Locate platelets.
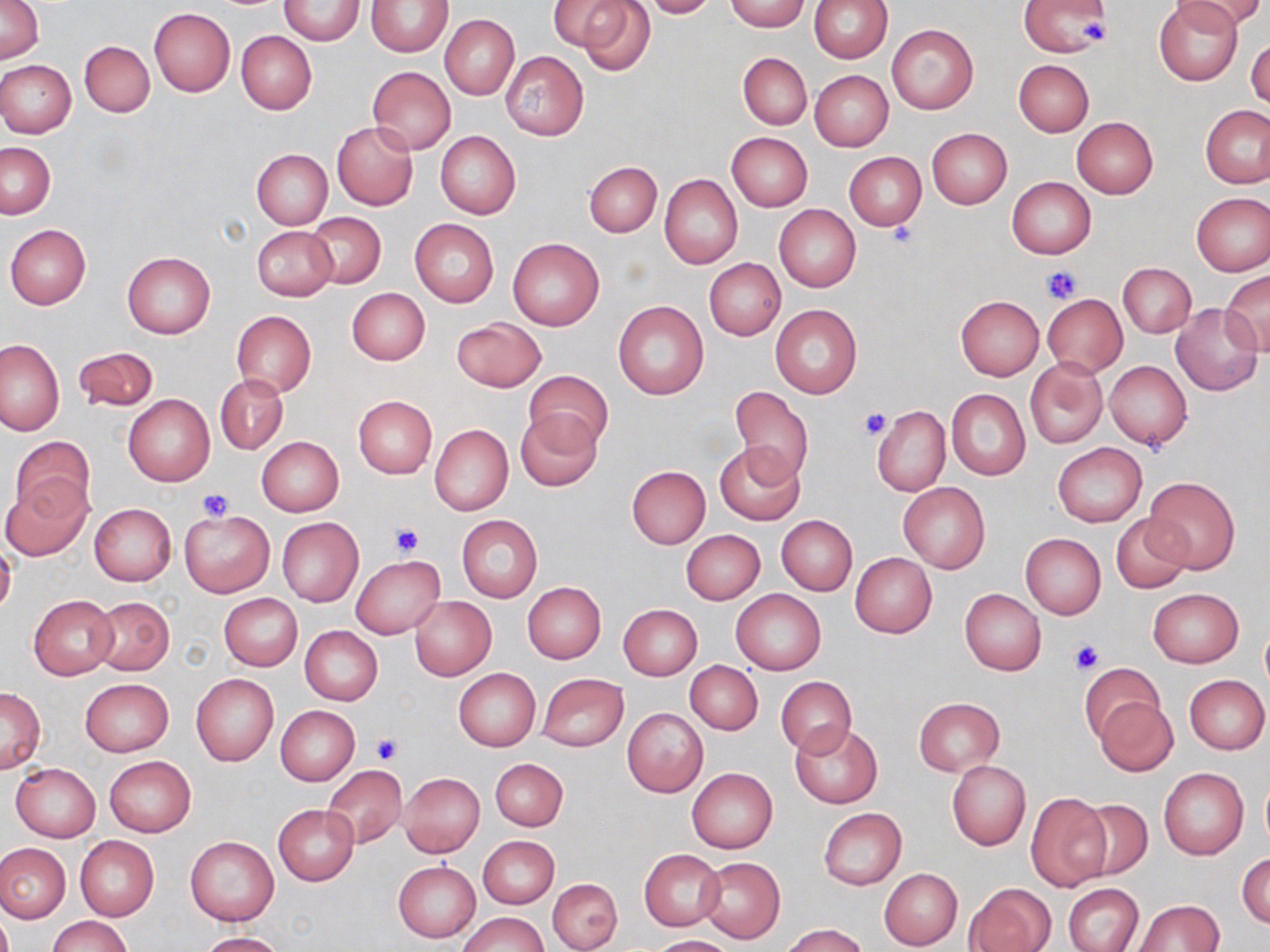

Approximate bounding boxes as named x1/y1/x2/y2 corners in pixels.
Platelets: (x1=1080, y1=18, x2=1107, y2=48), (x1=884, y1=223, x2=919, y2=251), (x1=1040, y1=264, x2=1081, y2=305), (x1=858, y1=408, x2=891, y2=441), (x1=199, y1=488, x2=233, y2=521), (x1=392, y1=523, x2=423, y2=556), (x1=1069, y1=640, x2=1104, y2=676), (x1=371, y1=734, x2=402, y2=764).

Summary:
  - Uninfected red blood cell locations: (x1=1, y1=0, x2=43, y2=64), (x1=278, y1=0, x2=366, y2=45), (x1=548, y1=0, x2=629, y2=52), (x1=576, y1=0, x2=656, y2=77), (x1=642, y1=0, x2=716, y2=18), (x1=723, y1=0, x2=810, y2=32), (x1=809, y1=0, x2=893, y2=62), (x1=1019, y1=0, x2=1114, y2=56), (x1=1177, y1=0, x2=1260, y2=34), (x1=366, y1=1, x2=451, y2=57), (x1=1152, y1=1, x2=1244, y2=85), (x1=149, y1=8, x2=235, y2=96), (x1=440, y1=15, x2=519, y2=99), (x1=887, y1=24, x2=978, y2=114), (x1=235, y1=30, x2=317, y2=114), (x1=1247, y1=34, x2=1269, y2=111), (x1=80, y1=41, x2=155, y2=117), (x1=501, y1=51, x2=589, y2=140), (x1=737, y1=53, x2=811, y2=128), (x1=0, y1=59, x2=76, y2=137), (x1=1014, y1=59, x2=1093, y2=136), (x1=367, y1=66, x2=456, y2=153), (x1=810, y1=70, x2=893, y2=151), (x1=1201, y1=106, x2=1269, y2=188), (x1=1071, y1=116, x2=1158, y2=198), (x1=331, y1=122, x2=419, y2=210), (x1=926, y1=127, x2=1012, y2=208), (x1=435, y1=132, x2=520, y2=219), (x1=727, y1=132, x2=812, y2=211), (x1=1, y1=142, x2=56, y2=218), (x1=252, y1=149, x2=332, y2=228), (x1=844, y1=152, x2=926, y2=229), (x1=583, y1=161, x2=662, y2=237), (x1=660, y1=174, x2=742, y2=268), (x1=1006, y1=177, x2=1096, y2=259), (x1=1192, y1=192, x2=1270, y2=276), (x1=774, y1=204, x2=861, y2=292), (x1=307, y1=213, x2=385, y2=288), (x1=409, y1=217, x2=499, y2=307), (x1=5, y1=224, x2=91, y2=309), (x1=251, y1=226, x2=338, y2=300), (x1=507, y1=238, x2=605, y2=330), (x1=122, y1=251, x2=216, y2=337), (x1=704, y1=258, x2=785, y2=341), (x1=1117, y1=262, x2=1196, y2=338), (x1=1221, y1=271, x2=1270, y2=357), (x1=346, y1=287, x2=430, y2=365), (x1=1042, y1=294, x2=1127, y2=377), (x1=955, y1=295, x2=1044, y2=380), (x1=613, y1=300, x2=709, y2=401), (x1=1170, y1=303, x2=1263, y2=396), (x1=770, y1=304, x2=862, y2=400), (x1=232, y1=311, x2=316, y2=398), (x1=451, y1=317, x2=546, y2=391), (x1=1, y1=338, x2=65, y2=435), (x1=73, y1=345, x2=159, y2=414), (x1=1025, y1=359, x2=1109, y2=450), (x1=1105, y1=361, x2=1191, y2=449), (x1=524, y1=370, x2=613, y2=455), (x1=216, y1=375, x2=288, y2=453), (x1=730, y1=387, x2=814, y2=486), (x1=946, y1=388, x2=1030, y2=480), (x1=123, y1=395, x2=214, y2=485), (x1=353, y1=396, x2=437, y2=478), (x1=872, y1=406, x2=950, y2=495), (x1=515, y1=411, x2=602, y2=491), (x1=430, y1=424, x2=513, y2=516), (x1=10, y1=436, x2=95, y2=520), (x1=257, y1=437, x2=344, y2=515), (x1=714, y1=442, x2=806, y2=525), (x1=1053, y1=442, x2=1146, y2=528), (x1=627, y1=466, x2=710, y2=548), (x1=1144, y1=475, x2=1240, y2=573), (x1=2, y1=479, x2=91, y2=561), (x1=898, y1=482, x2=990, y2=573), (x1=89, y1=503, x2=176, y2=585), (x1=180, y1=509, x2=274, y2=596), (x1=1111, y1=513, x2=1193, y2=593), (x1=456, y1=516, x2=541, y2=602), (x1=776, y1=516, x2=858, y2=596), (x1=278, y1=518, x2=363, y2=605), (x1=681, y1=530, x2=765, y2=604), (x1=1020, y1=533, x2=1106, y2=619), (x1=0, y1=544, x2=17, y2=619), (x1=849, y1=552, x2=937, y2=639), (x1=352, y1=556, x2=445, y2=640), (x1=522, y1=582, x2=605, y2=663), (x1=1148, y1=588, x2=1244, y2=667), (x1=731, y1=589, x2=826, y2=674), (x1=960, y1=589, x2=1046, y2=675), (x1=219, y1=594, x2=301, y2=670), (x1=30, y1=595, x2=117, y2=678), (x1=90, y1=596, x2=175, y2=675), (x1=410, y1=597, x2=496, y2=679), (x1=618, y1=604, x2=703, y2=679), (x1=1259, y1=623, x2=1270, y2=697), (x1=299, y1=626, x2=382, y2=706), (x1=686, y1=661, x2=763, y2=734), (x1=1079, y1=661, x2=1162, y2=744), (x1=453, y1=668, x2=540, y2=751), (x1=191, y1=673, x2=278, y2=765), (x1=538, y1=673, x2=629, y2=752), (x1=1185, y1=674, x2=1269, y2=754), (x1=775, y1=676, x2=857, y2=757), (x1=80, y1=679, x2=174, y2=757), (x1=1, y1=687, x2=46, y2=772), (x1=1095, y1=696, x2=1178, y2=776), (x1=913, y1=697, x2=1004, y2=775), (x1=276, y1=706, x2=360, y2=785), (x1=622, y1=707, x2=707, y2=797), (x1=790, y1=721, x2=882, y2=808), (x1=103, y1=755, x2=196, y2=838), (x1=490, y1=758, x2=568, y2=830), (x1=946, y1=760, x2=1031, y2=850), (x1=10, y1=763, x2=100, y2=841), (x1=322, y1=765, x2=407, y2=849), (x1=1159, y1=767, x2=1248, y2=859), (x1=687, y1=768, x2=777, y2=853), (x1=398, y1=772, x2=484, y2=857), (x1=1260, y1=774, x2=1270, y2=848), (x1=1025, y1=792, x2=1112, y2=892), (x1=1078, y1=798, x2=1152, y2=881), (x1=273, y1=804, x2=359, y2=886), (x1=817, y1=808, x2=906, y2=890), (x1=75, y1=836, x2=158, y2=921), (x1=186, y1=836, x2=278, y2=925), (x1=478, y1=836, x2=559, y2=908), (x1=0, y1=842, x2=70, y2=923), (x1=639, y1=849, x2=726, y2=930), (x1=1237, y1=853, x2=1270, y2=929), (x1=697, y1=857, x2=785, y2=943), (x1=393, y1=861, x2=481, y2=942), (x1=879, y1=868, x2=963, y2=950), (x1=548, y1=878, x2=621, y2=951), (x1=965, y1=883, x2=1056, y2=952), (x1=1064, y1=884, x2=1143, y2=952), (x1=1134, y1=900, x2=1224, y2=951), (x1=460, y1=912, x2=548, y2=952), (x1=48, y1=916, x2=133, y2=952), (x1=782, y1=923, x2=868, y2=952), (x1=197, y1=932, x2=287, y2=952), (x1=648, y1=935, x2=736, y2=952)
  - Slide-level diagnosis: negative for blood parasites
  - Modality: optical microscopy
  - Image size: 1270×952 pixels
  - Field of view: single
  - Stain: May-Grünwald-Giemsa
  - Magnification: 1000x
  - Preparation: thin blood smear